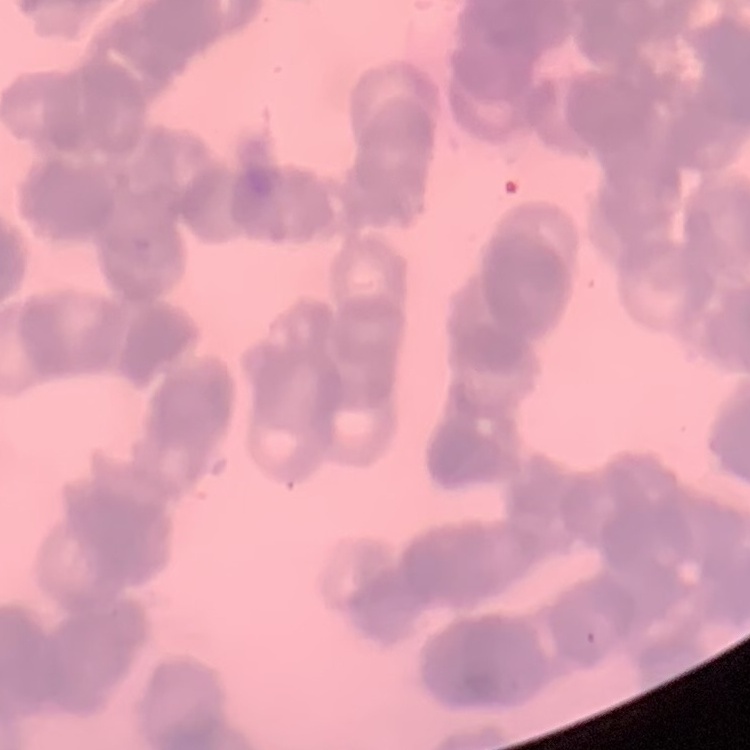
red blood cell morphology = rouleaux formation
stain = Field's or Giemsa
preparation = thin blood smear
image type = square crop of a larger photomicrograph